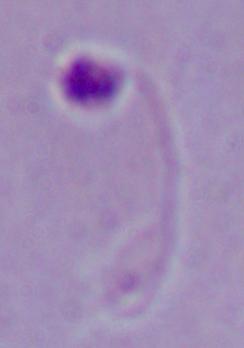
Summary:
  - Modality: photomicrograph
  - Identification: Leishmania
  - Magnification: 1000x